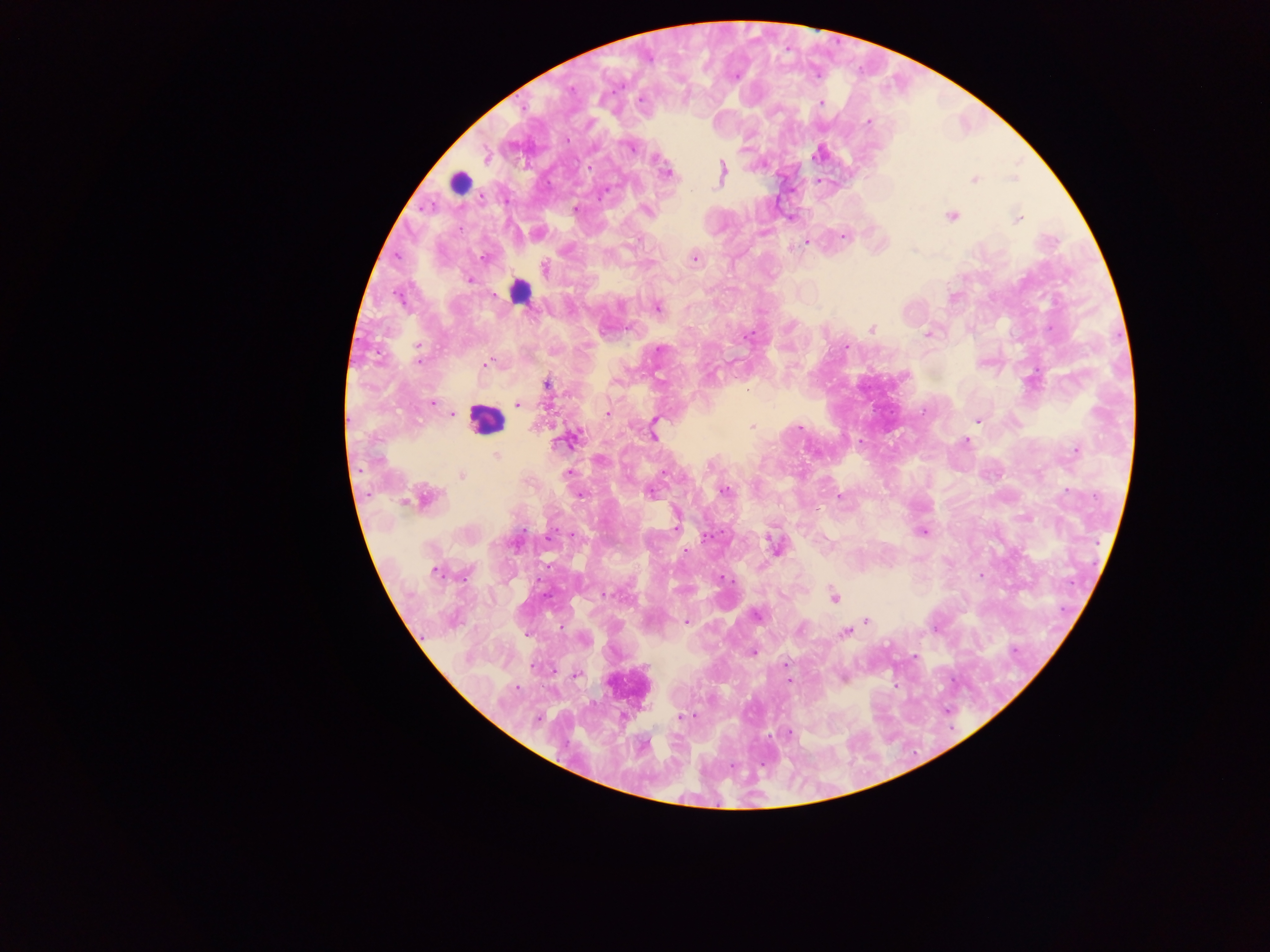
image size = 1270×952 pixels
country = Ghana
leukocyte locations = approximate centers as {x, y} in pixels: {461, 183}, {520, 290}, {485, 420}, {628, 686}
malaria parasite locations = approximate centers as {x, y} in pixels: {734, 76}, {640, 100}, {821, 103}, {868, 122}, {630, 146}, {818, 153}, {666, 172}, {722, 173}, {973, 179}, {820, 181}, {576, 209}, {646, 211}, {951, 215}, {790, 217}, {1017, 218}, {763, 232}, {537, 233}, {843, 235}, {806, 242}, {694, 257}, {484, 258}, {543, 269}, {469, 279}, {656, 307}, {870, 328}, {928, 333}, {845, 346}, {486, 364}, {546, 383}, {432, 403}, {518, 404}, {607, 413}, {452, 415}, {978, 420}, {752, 426}, {798, 426}, {653, 432}, {570, 439}, {965, 442}, {1076, 449}, {495, 455}, {600, 459}, {663, 472}, {566, 474}, {461, 475}, {724, 490}, {650, 492}, {581, 494}, {838, 497}, {419, 498}, {1026, 518}, {923, 531}, {775, 546}, {686, 552}, {435, 570}, {979, 576}, {720, 578}, {834, 596}, {755, 614}, {687, 621}, {865, 621}, {935, 627}, {844, 632}, {582, 639}, {753, 651}, {915, 657}, {785, 664}, {575, 674}, {842, 677}, {788, 680}, {679, 717}, {694, 717}, {789, 734}, {732, 765}
preparation = thick blood smear
capture = mobile-phone photograph through a microscope
field of view = single